Describe the morphology of the red blood cells.
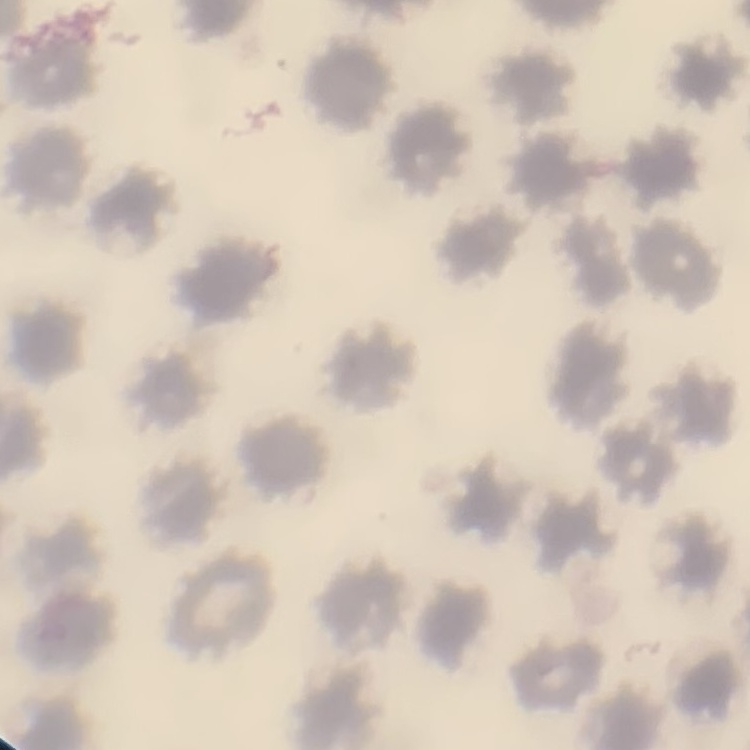

No rouleaux formation.

Thin peripheral smear. Square crop of a larger photomicrograph. Stained with either Field's or Giemsa.